Report the malaria status of this cell.
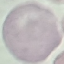
It is uninfected.

preparation = thin blood film
capture = smartphone camera at the microscope eyepiece
image type = cell patch, automatically extracted from a larger field of view and resized to 64 × 64 pixels
stain = Giemsa